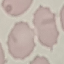
Malaria status: uninfected. Giemsa-stained preparation. Cell patch, automatically extracted from a larger field of view and resized to 64 × 64 pixels. Thin blood film. Acquired by smartphone through the microscope eyepiece.